Describe the morphology of the red blood cells.
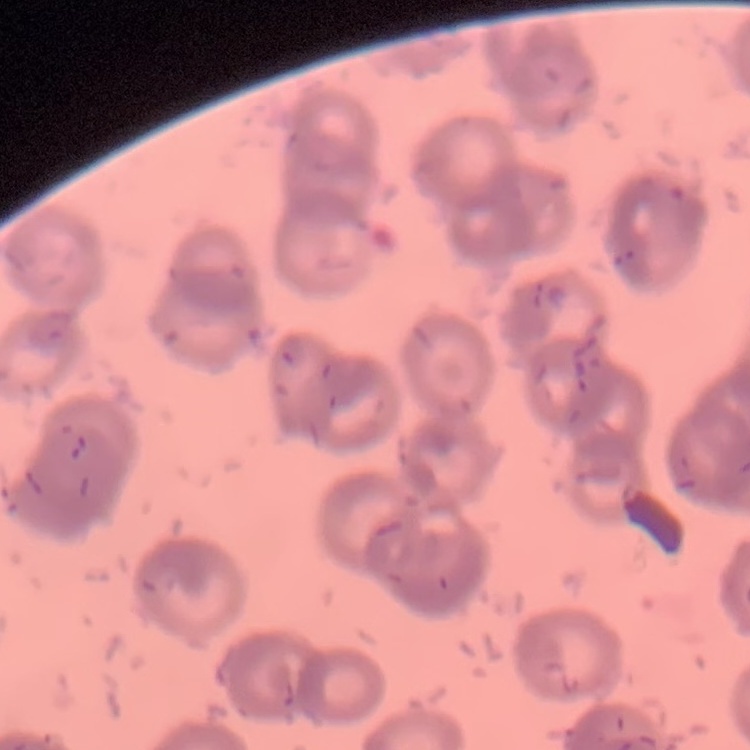
Rouleaux formation.

stain: Field's or Giemsa
image_type: one tile cut from a larger photomicrograph
preparation: thin peripheral smear